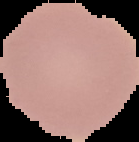

Malaria status: uninfected. Cell region segmented out of the field of view; the surrounding area is masked to black. From a thin blood film. Image is 139×142 pixels.